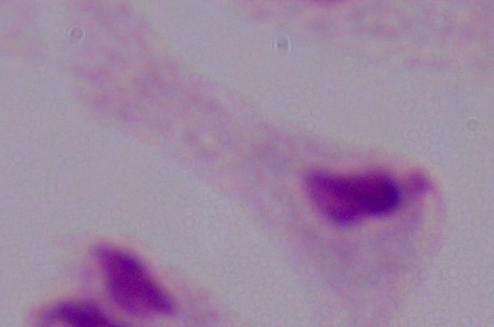

{
  "identification": "trichomonad",
  "modality": "micrograph",
  "magnification": "1000x"
}